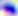
Summary:
  - Identification: Toxoplasma gondii
  - Magnification: 400x
  - Modality: micrograph